Comment on the morphology of the red blood cells.
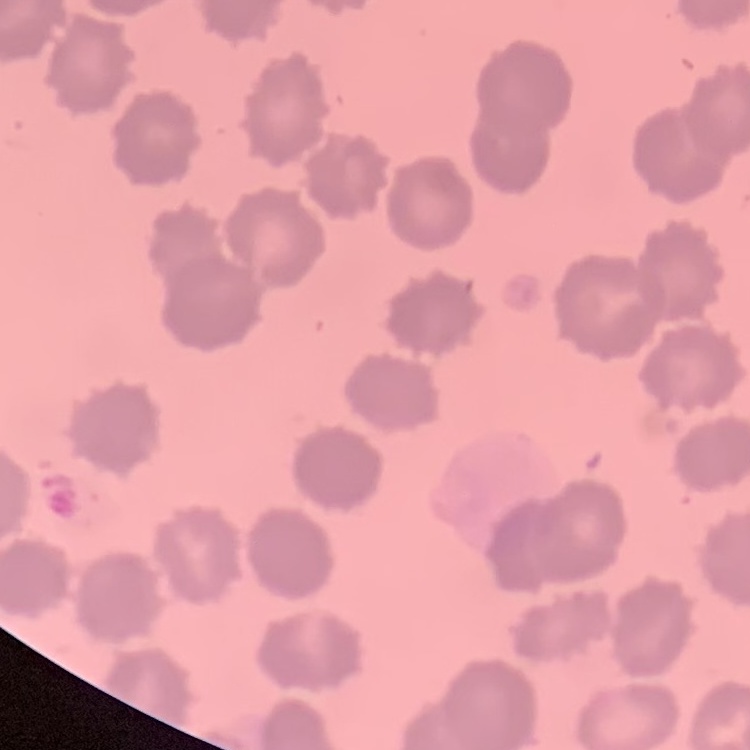
No rouleaux formation.

Square crop of a larger photomicrograph. Thin blood smear. Stained with either Field's or Giemsa.